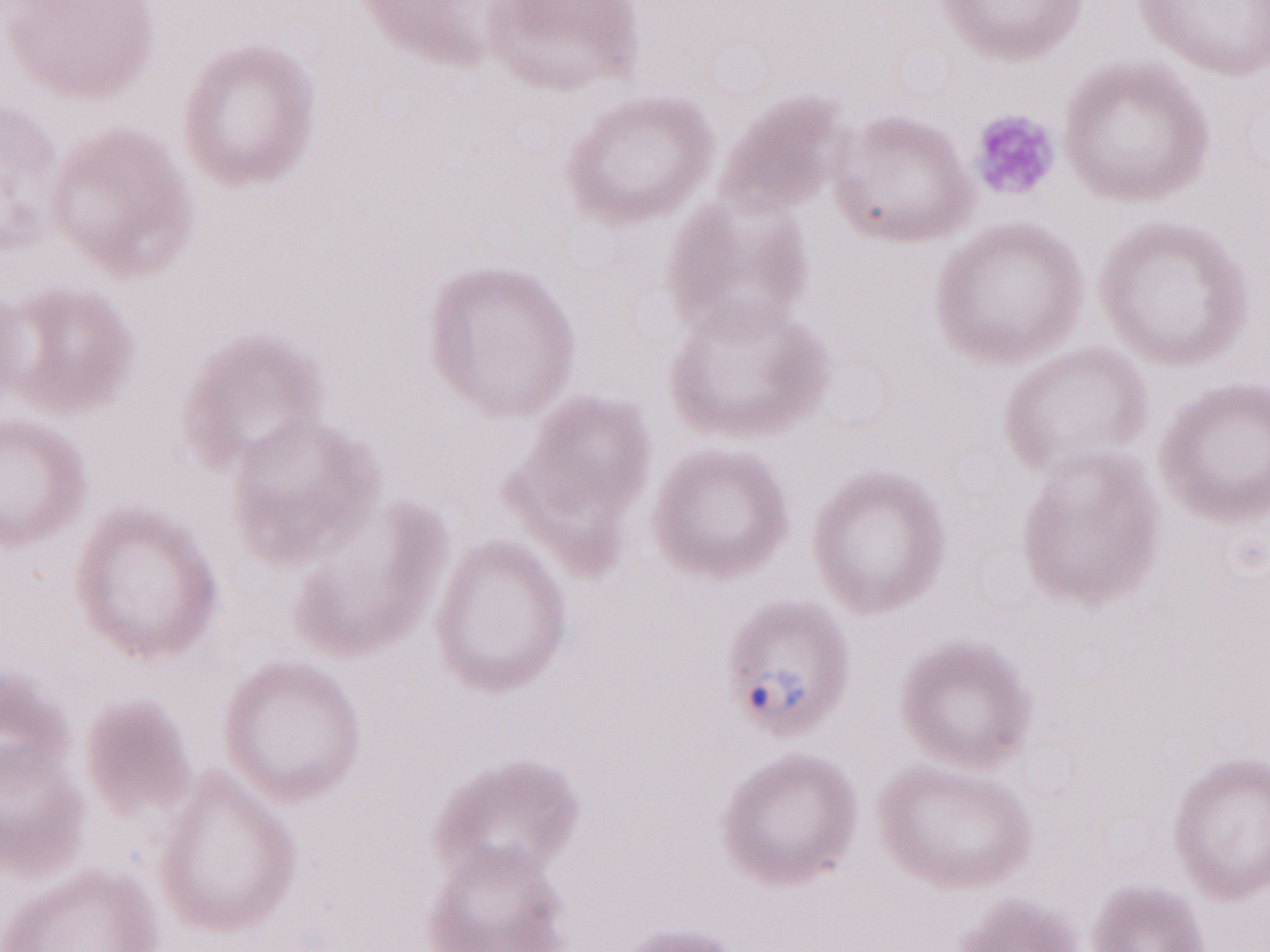
Magnification: 1,000x. Thin peripheral-blood smear. Image is 1270×952 pixels. Patient-level malaria diagnosis: positive. Olympus BX43 microscope and DP73 digital camera. One field of this slide. May-Grünwald-Giemsa stain.